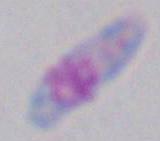

{
  "modality": "micrograph",
  "magnification": "1000x",
  "identification": "Toxoplasma gondii"
}